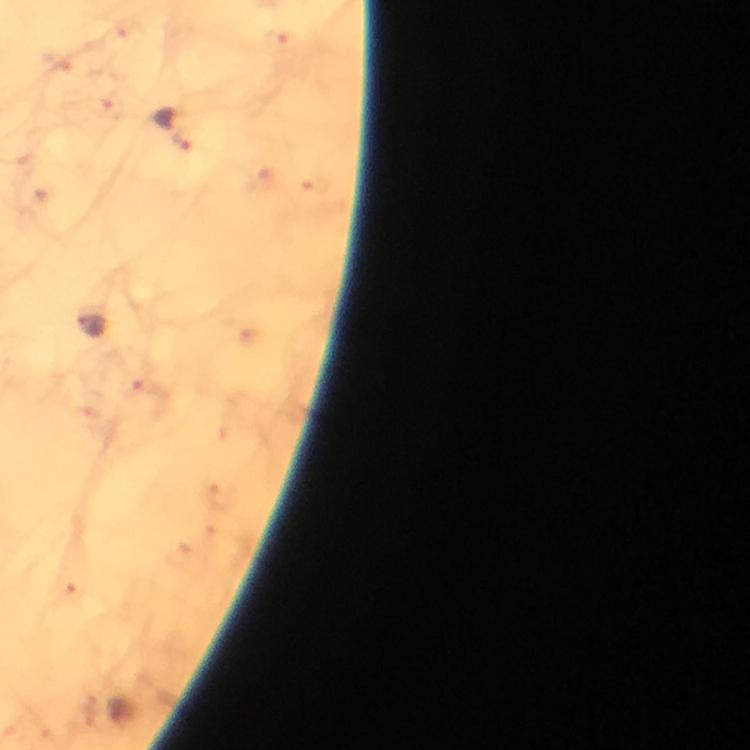 Approximate centers as [x, y] in pixels. Malaria parasite locations: [175, 127], [91, 323]. A crop from one field of view. Photographed through the microscope with a smartphone camera. Thick smear. Immersion oil applied. 100x magnification. From a malaria diagnostic workup. Giemsa-stained preparation. Image is 750×750 pixels.